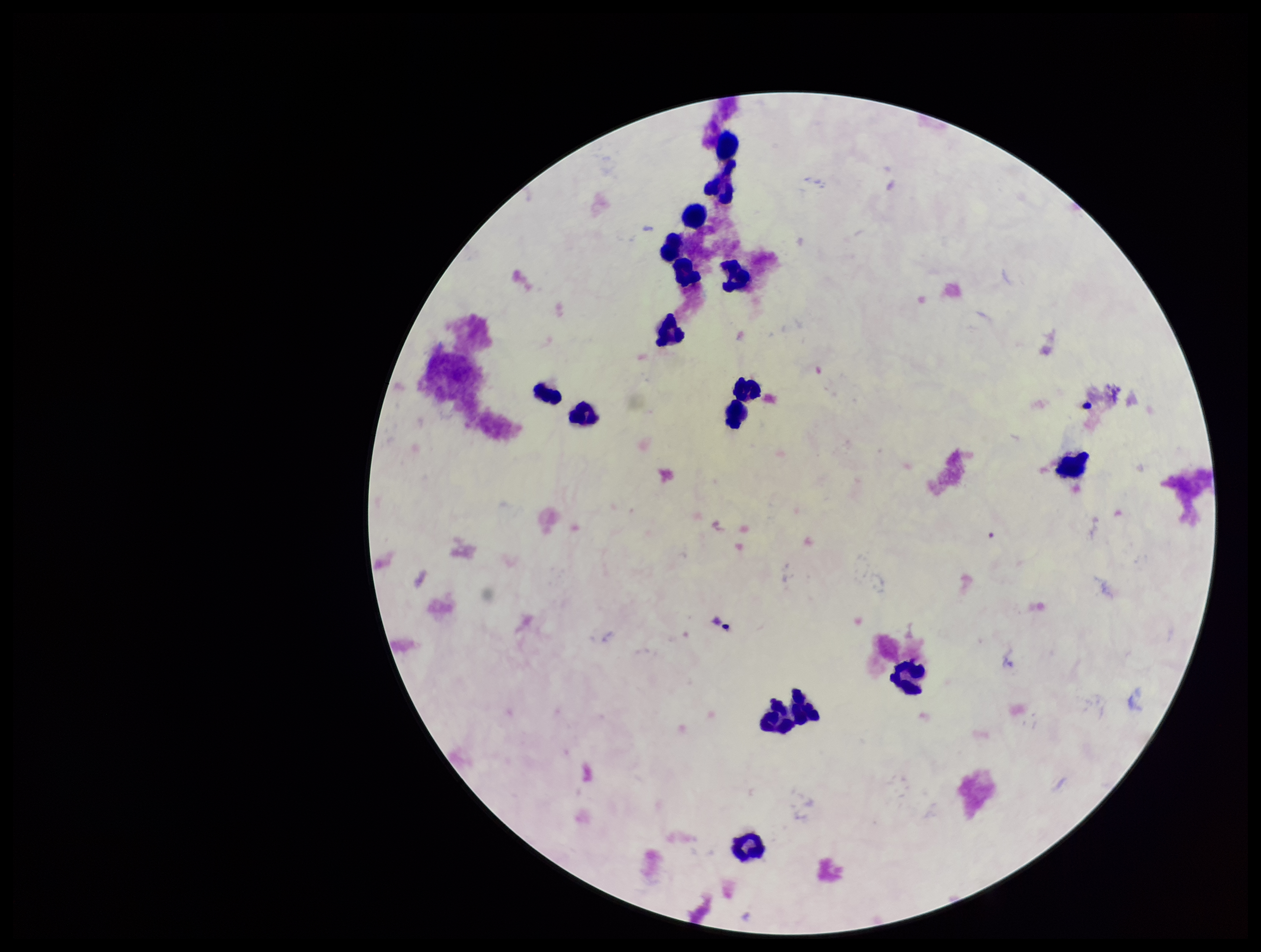
Summary:
  - Stain: Giemsa
  - Field of view: one from this slide
  - Parasite count: 0
  - Patient malaria status: negative
  - Image size: 1261×952 pixels
  - Plasmodium parasites: none identified
  - Leukocyte count: 16
  - Capture: smartphone photograph through the microscope eyepiece
  - Preparation: thick